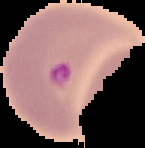

image type = cell region segmented out of the field of view; surrounding area masked to black
image size = 145×148 pixels
preparation = thin blood smear
malaria status = parasitized